Give the position of every malaria parasite.
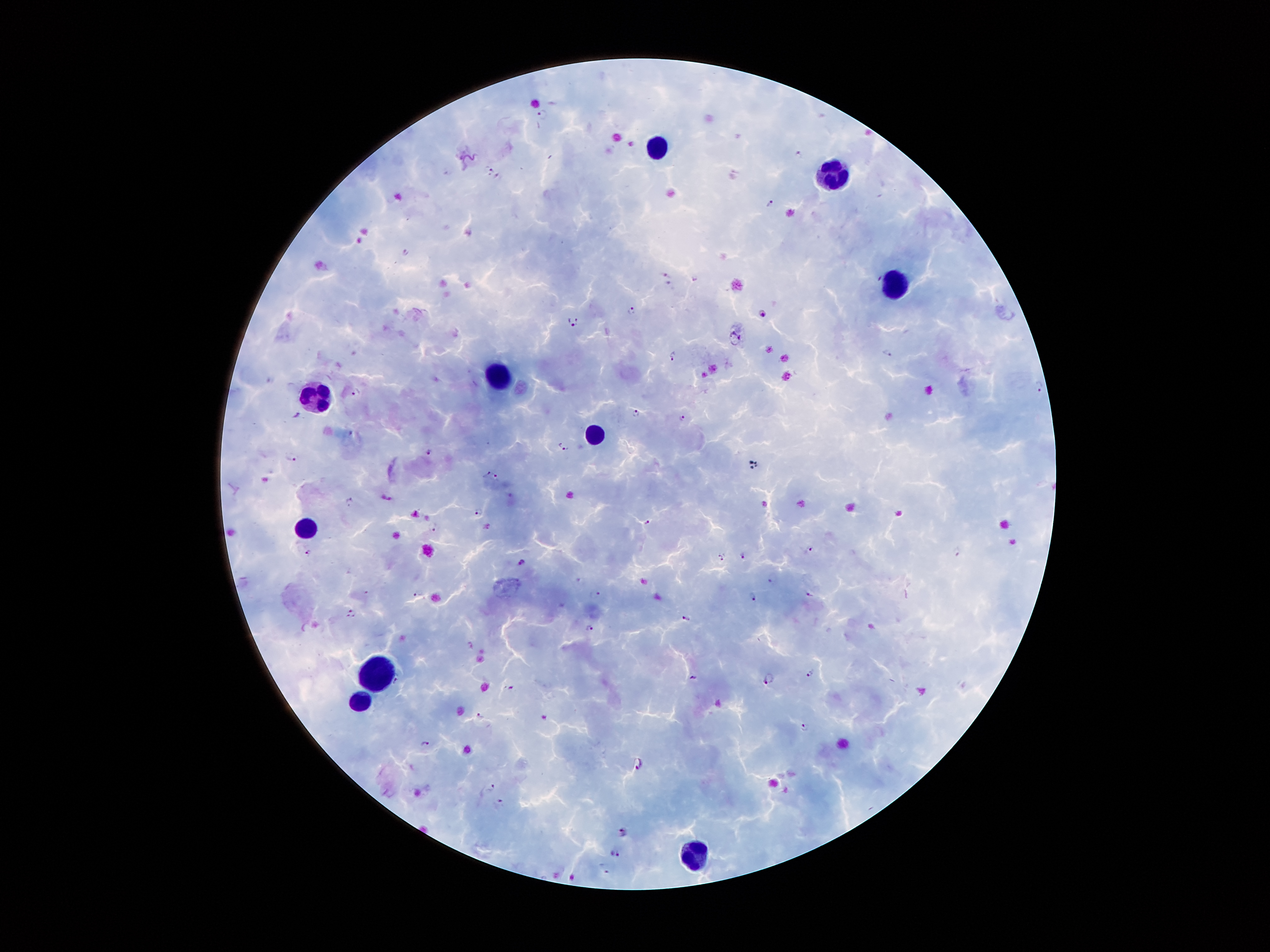
Approximate centers as {x, y} in pixels.
Malaria parasites: {543, 114}, {798, 154}, {489, 168}, {497, 176}, {770, 202}, {406, 254}, {667, 275}, {631, 309}, {763, 314}, {573, 322}, {735, 338}, {887, 354}, {672, 355}, {1039, 387}, {356, 392}, {635, 412}, {299, 415}, {681, 417}, {563, 448}, {429, 449}, {292, 457}, {492, 475}, {350, 502}, {479, 512}, {649, 523}, {432, 526}, {807, 548}, {308, 552}, {957, 552}, {722, 557}, {744, 557}, {522, 561}, {771, 579}, {808, 592}, {596, 594}, {418, 595}, {753, 596}, {352, 613}, {687, 618}, {589, 628}, {810, 673}, {769, 677}, {695, 678}, {398, 680}, {512, 687}, {480, 715}, {804, 728}, {424, 743}, {639, 763}, {491, 786}, {500, 801}, {621, 832}, {616, 854}, {605, 867}.

Summary:
  - Leukocyte locations: {659, 150}, {836, 168}, {899, 282}, {501, 375}, {313, 394}, {592, 429}, {309, 528}, {381, 675}, {357, 703}, {697, 854}
  - Field of view: one from this slide
  - Patient malaria status: infected with Plasmodium falciparum
  - Preparation: thick peripheral-blood smear
  - Magnification: 100x
  - Image size: 1270×952 pixels
  - Stain: Giemsa
  - Capture: smartphone camera through the microscope eyepiece